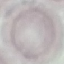
Summary:
  - Result: no malaria parasites detected
  - Image type: cell patch, automatically extracted from a larger field of view and resized to 64 × 64 pixels
  - Stain: Giemsa
  - Preparation: thin blood smear
  - Capture: smartphone camera at the microscope eyepiece